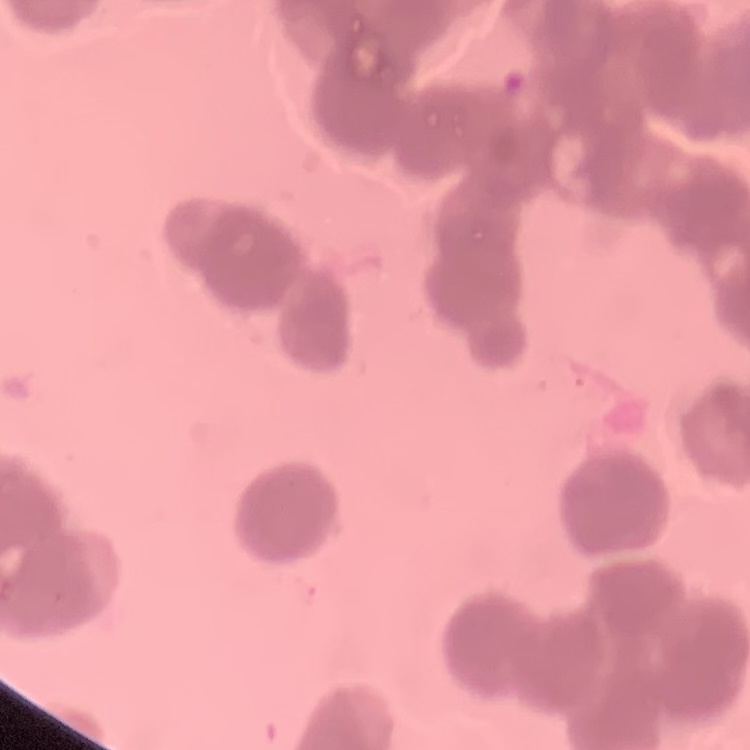
red_blood_cell_morphology: rouleaux formation
image_type: square crop of a larger photomicrograph
preparation: thin peripheral smear
stain: Field's or Giemsa